Give the extent of all Babesia divergens-infected red blood cells.
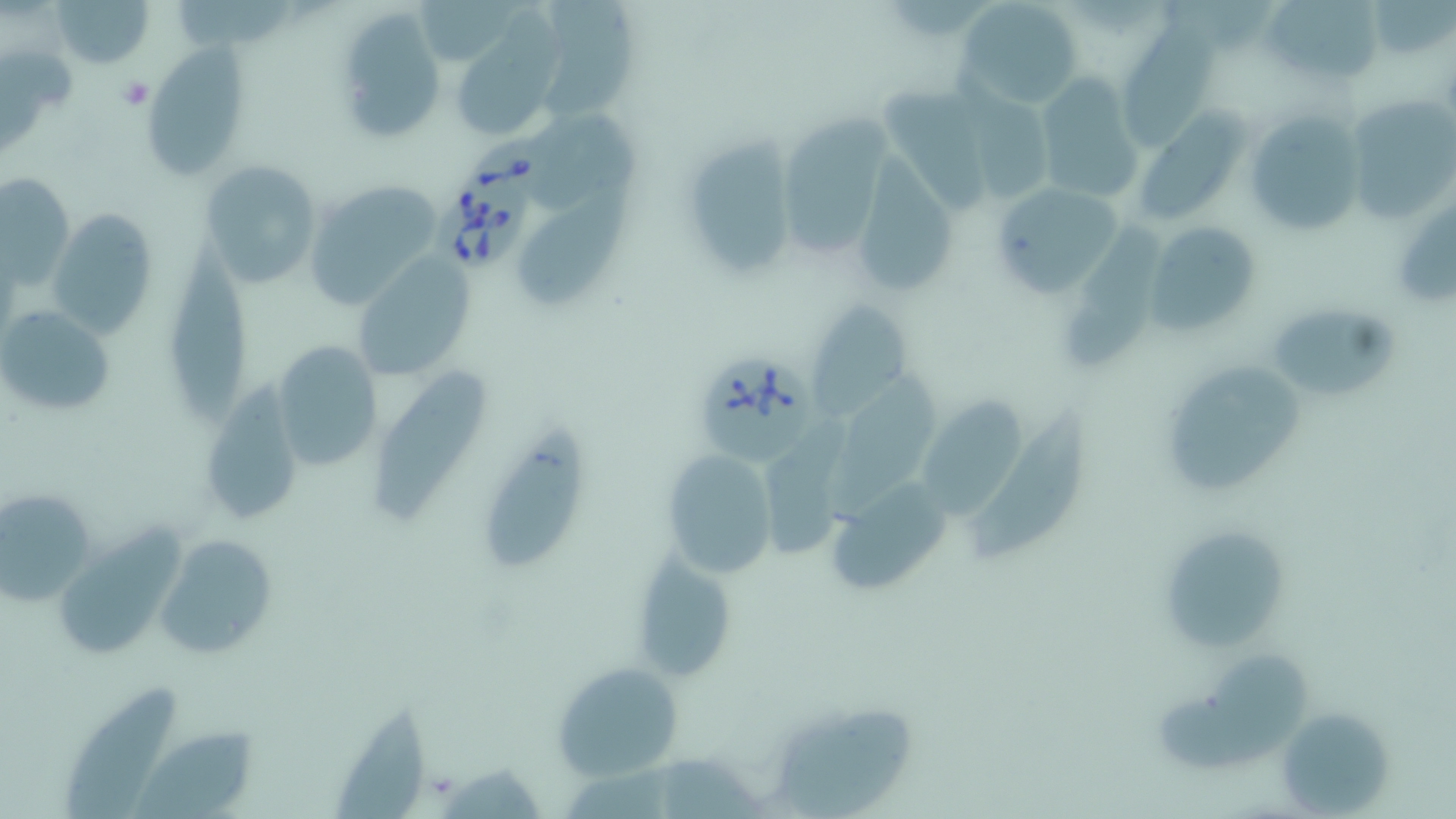
Approximate bounding boxes as named x1/y1/x2/y2 corners in pixels.
Babesia divergens-infected red blood cells: (x1=459, y1=135, x2=556, y2=209), (x1=431, y1=182, x2=536, y2=273), (x1=695, y1=350, x2=814, y2=464).

slide_level_diagnosis: Babesia divergens
platelet_locations: 'approximate bounding boxes as named x1/y1/x2/y2 corners in pixels: (x1=119, y1=79, x2=152, y2=110)'
modality: optical microscopy
uninfected_red_blood_cell_locations: 'approximate bounding boxes as named x1/y1/x2/y2 corners in pixels: (x1=49, y1=0, x2=157, y2=68), (x1=955, y1=0, x2=1084, y2=109), (x1=1263, y1=0, x2=1383, y2=87), (x1=176, y1=1, x2=300, y2=54), (x1=543, y1=1, x2=642, y2=127), (x1=1367, y1=1, x2=1451, y2=59), (x1=332, y1=8, x2=447, y2=146), (x1=458, y1=11, x2=567, y2=138), (x1=1117, y1=16, x2=1222, y2=153), (x1=0, y1=46, x2=76, y2=156), (x1=141, y1=46, x2=248, y2=180), (x1=1031, y1=75, x2=1142, y2=205), (x1=1345, y1=94, x2=1456, y2=228), (x1=783, y1=103, x2=898, y2=261), (x1=1242, y1=109, x2=1362, y2=238), (x1=529, y1=112, x2=645, y2=212), (x1=1136, y1=113, x2=1242, y2=225), (x1=689, y1=124, x2=792, y2=279), (x1=861, y1=144, x2=961, y2=300), (x1=200, y1=161, x2=324, y2=289), (x1=2, y1=174, x2=74, y2=284), (x1=303, y1=178, x2=443, y2=306), (x1=989, y1=181, x2=1123, y2=298), (x1=522, y1=189, x2=631, y2=311), (x1=1062, y1=207, x2=1168, y2=376), (x1=45, y1=208, x2=157, y2=339), (x1=1145, y1=220, x2=1263, y2=336), (x1=167, y1=231, x2=251, y2=430), (x1=351, y1=252, x2=475, y2=377), (x1=807, y1=298, x2=917, y2=416), (x1=1266, y1=302, x2=1397, y2=403), (x1=1, y1=305, x2=116, y2=419), (x1=268, y1=339, x2=387, y2=473), (x1=1157, y1=360, x2=1301, y2=501), (x1=371, y1=366, x2=489, y2=524), (x1=836, y1=373, x2=937, y2=522), (x1=196, y1=386, x2=304, y2=528), (x1=924, y1=392, x2=1023, y2=519), (x1=969, y1=400, x2=1091, y2=566), (x1=767, y1=420, x2=859, y2=558), (x1=477, y1=432, x2=595, y2=576), (x1=659, y1=449, x2=779, y2=580), (x1=822, y1=477, x2=956, y2=598), (x1=0, y1=488, x2=100, y2=604), (x1=57, y1=512, x2=184, y2=663), (x1=1157, y1=524, x2=1291, y2=655), (x1=154, y1=535, x2=274, y2=658), (x1=628, y1=552, x2=738, y2=681), (x1=1154, y1=648, x2=1313, y2=774), (x1=552, y1=657, x2=685, y2=782), (x1=64, y1=683, x2=176, y2=817), (x1=330, y1=699, x2=434, y2=816), (x1=765, y1=701, x2=923, y2=816), (x1=1275, y1=706, x2=1393, y2=816), (x1=136, y1=718, x2=253, y2=817)'
image_size: 1456×819 pixels
field_of_view: one of a larger specimen
magnification: 1000x
stain: May-Grünwald-Giemsa
preparation: thin blood film